Look for Plasmodium parasites.
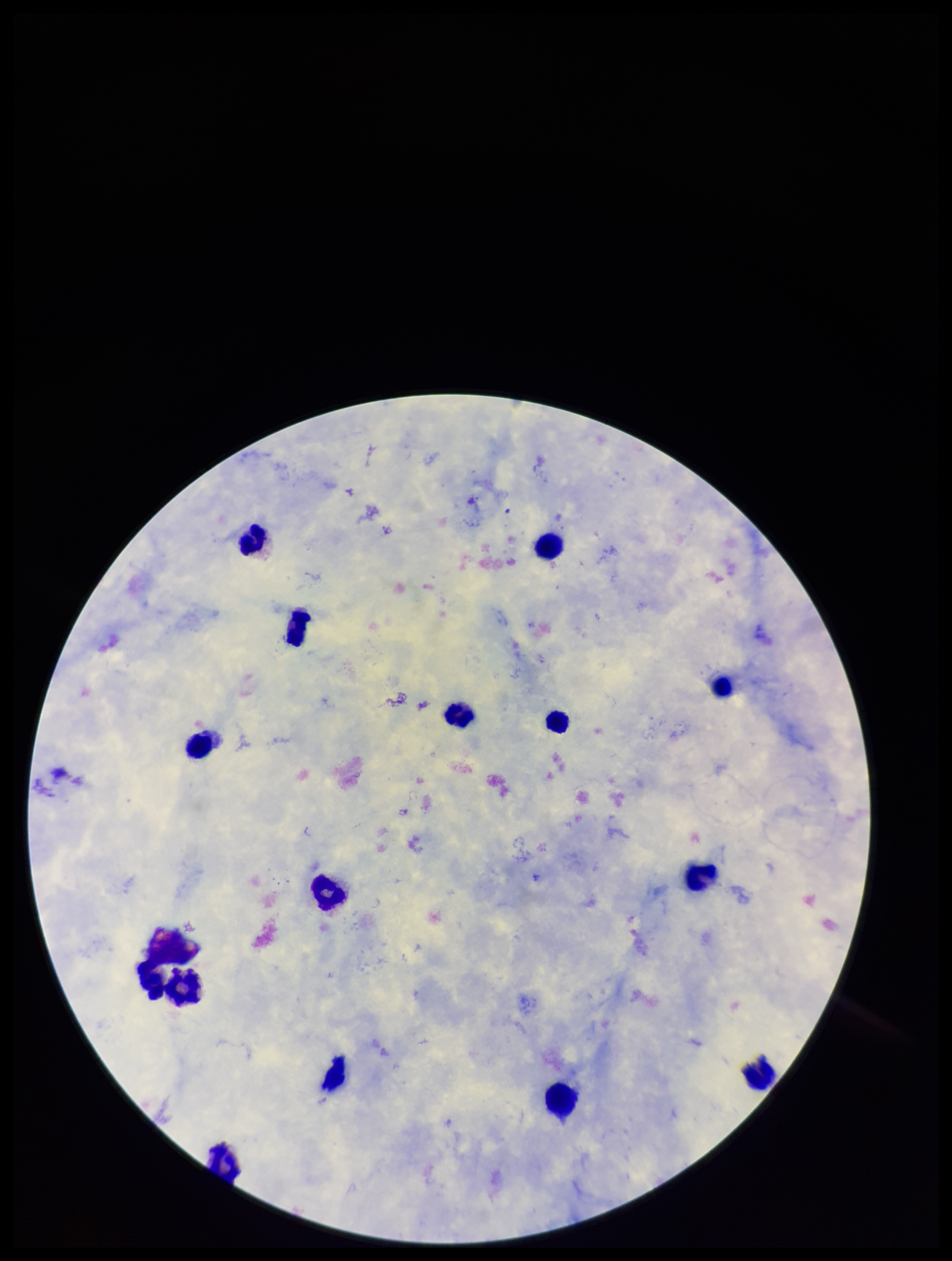
None detected.

image size = 952×1261 pixels
species reported for this patient = Plasmodium falciparum
capture = smartphone photograph through the microscope eyepiece
preparation = thick smear
leukocyte count = 15
stain = Giemsa
parasite count = 0
field of view = single
patient malaria status = infected